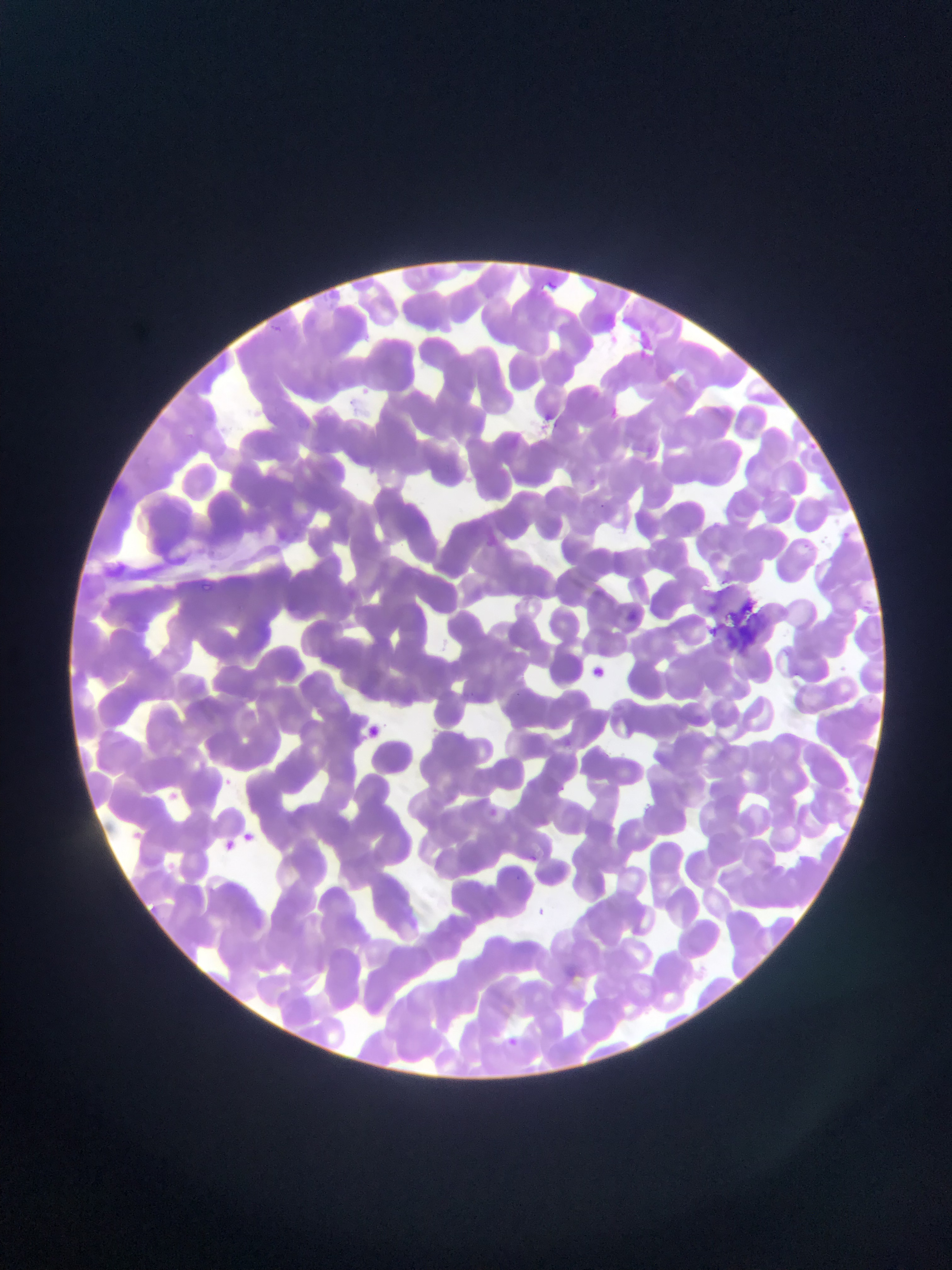
image_size: 952×1270 pixels
country: Ghana
preparation: thin blood smear
malaria_parasite_locations: 'approximate bounding boxes as [left, top, right, bottom] in pixels: [627, 605, 650, 634], [594, 661, 613, 687], [360, 719, 394, 754], [216, 777, 228, 786], [218, 835, 249, 863]'
field_of_view: single
capture: mobile-phone photograph through a microscope